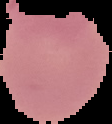

Summary:
  - Image type: segmented cell region on a black background
  - Image size: 112×124 pixels
  - Result: no Plasmodium parasites detected
  - Preparation: thin blood film